Identify the preparation type.
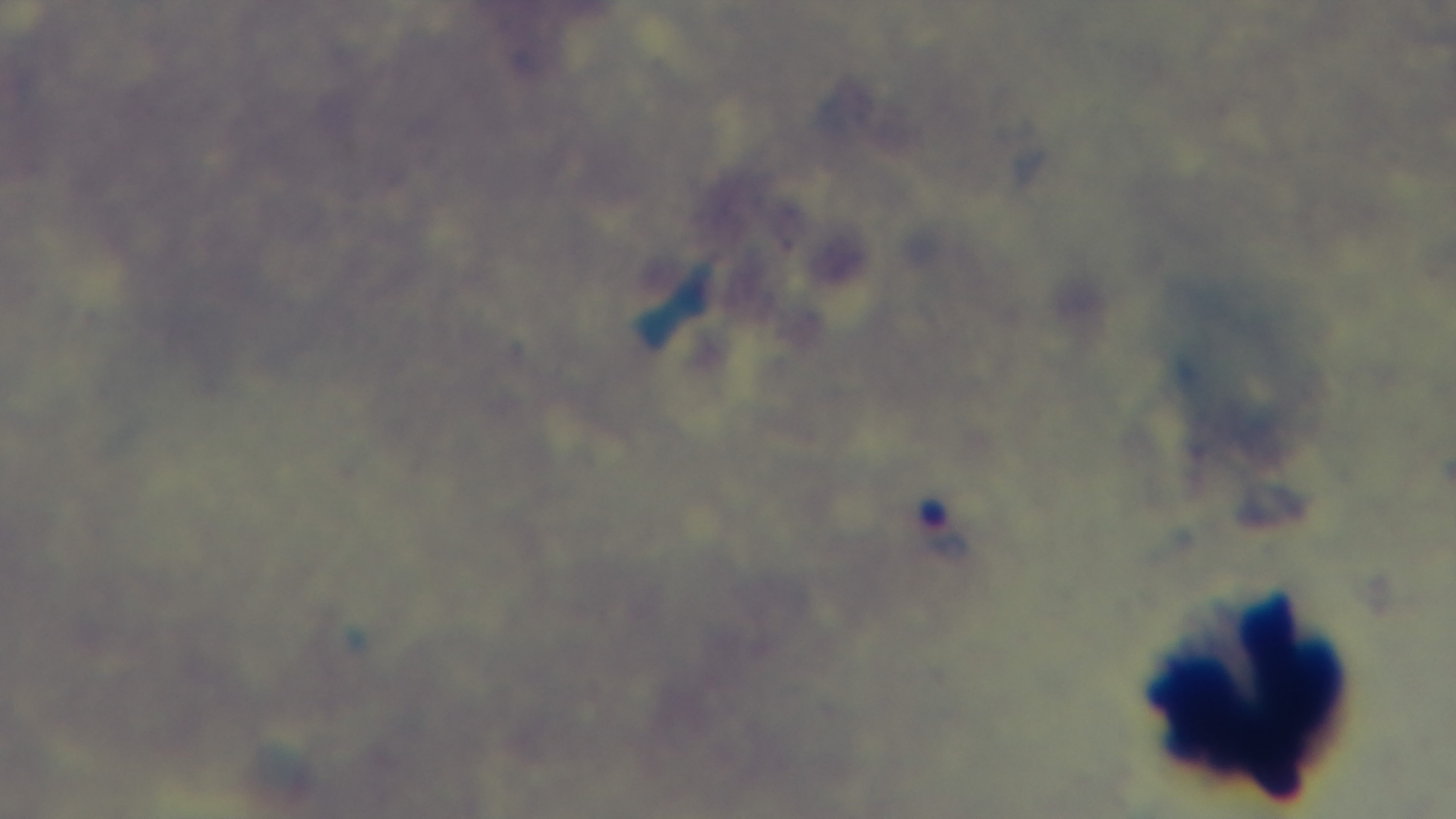

It is a thick blood film.

stain = Giemsa
field of view = single
modality = light microscopy
objective = 100x oil immersion
capture = mounted 4K digital camera
malaria status = infected